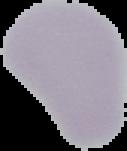
image size = 127×151 pixels
preparation = thin blood film
malaria status = uninfected
image type = segmented cell region on a black background